Locate every Plasmodium parasite and every leukocyte.
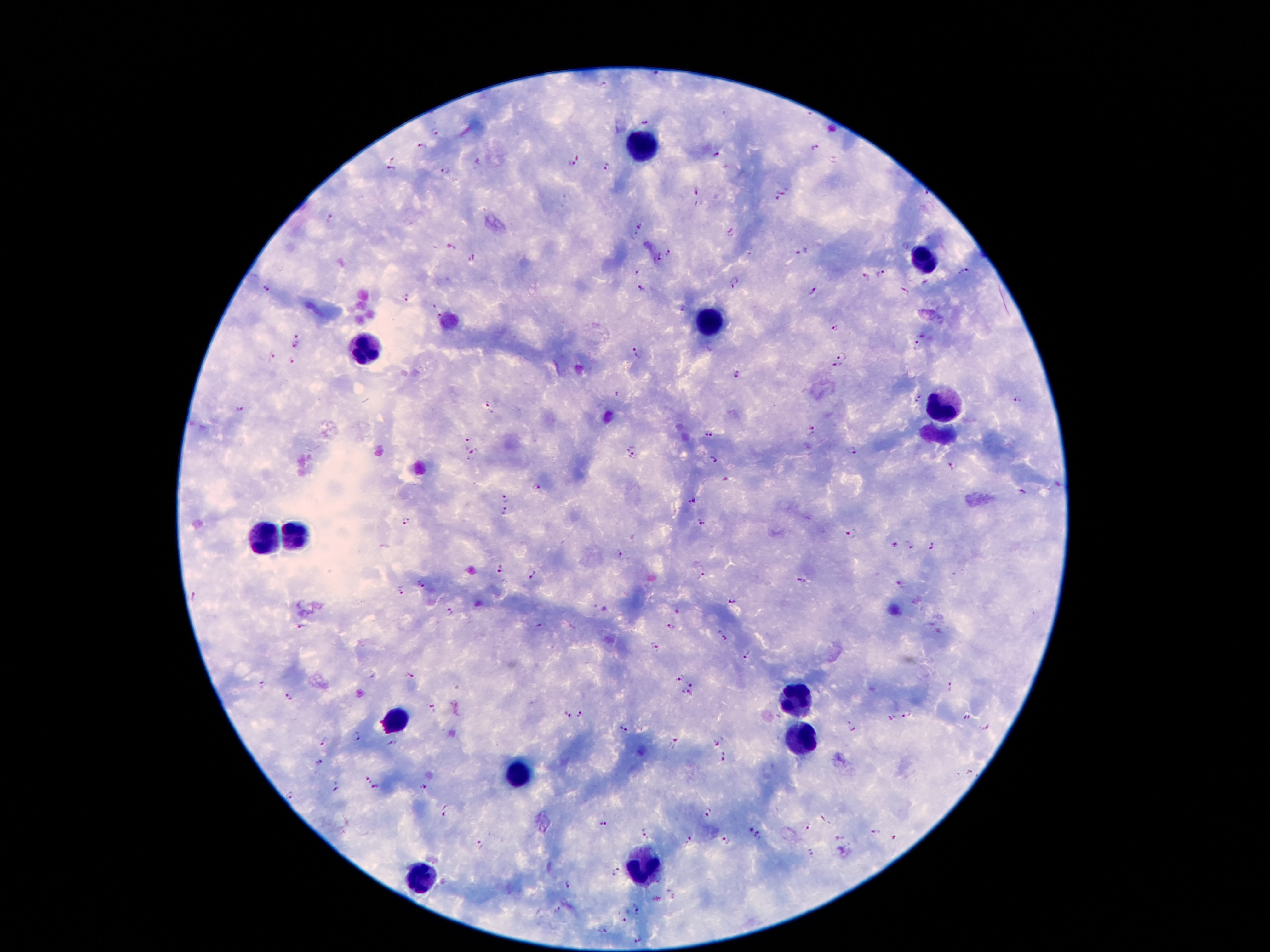
Approximate centers as (x, y) in pixels.
Plasmodium parasites: (603, 85), (643, 120), (436, 129), (422, 144), (815, 146), (716, 155), (391, 157), (478, 161), (834, 161), (571, 162), (606, 167), (390, 170), (443, 172), (694, 189), (784, 191), (776, 198), (700, 204), (640, 226), (730, 233), (633, 235), (451, 248), (802, 250), (670, 252), (471, 258), (659, 258), (635, 272), (963, 272), (881, 273), (864, 276), (736, 282), (266, 289), (640, 289), (813, 291), (904, 292), (406, 295), (681, 308), (436, 309), (835, 327), (922, 333), (298, 334), (296, 344), (914, 344), (636, 353), (843, 354), (270, 357), (292, 361), (836, 364), (737, 375), (921, 392), (1017, 399), (913, 402), (489, 407), (237, 409), (812, 431), (707, 433), (464, 443), (630, 446), (851, 451), (475, 456), (634, 456), (714, 459), (950, 466), (537, 486), (1023, 493), (506, 496), (693, 501), (503, 511), (403, 522), (702, 524), (852, 532), (910, 543), (895, 544), (931, 546), (620, 555), (501, 569), (703, 574), (535, 576), (801, 581), (422, 584), (903, 584), (401, 590), (733, 601), (449, 610), (301, 626), (538, 626), (671, 627), (725, 638), (655, 648), (748, 655), (676, 676), (411, 677), (691, 684), (263, 685), (950, 688), (680, 691), (689, 693), (290, 697), (431, 709), (908, 714), (566, 715), (582, 715), (891, 718), (966, 718), (851, 726), (623, 727), (985, 728), (357, 738), (324, 742), (716, 742), (393, 744), (675, 744), (723, 755), (319, 762), (367, 780), (337, 786), (375, 788), (422, 789), (291, 795), (446, 811), (706, 811), (603, 825), (806, 827), (749, 829), (875, 831), (646, 834), (839, 837), (758, 838), (690, 839), (724, 841), (480, 844), (808, 852), (615, 870), (568, 883), (672, 894), (637, 908), (556, 910), (623, 921), (603, 929), (638, 939).
Leukocytes: (642, 147), (926, 253), (706, 319), (360, 357), (941, 403), (298, 534), (261, 539), (795, 702), (395, 720), (798, 742), (516, 777), (642, 868), (417, 878).

Summary:
  - Preparation: thick blood smear
  - Magnification: 100x
  - Image size: 1270×952 pixels
  - Capture: smartphone camera through the microscope eyepiece
  - Field of view: single
  - Stain: Giemsa
  - Patient malaria status: infected with Plasmodium falciparum